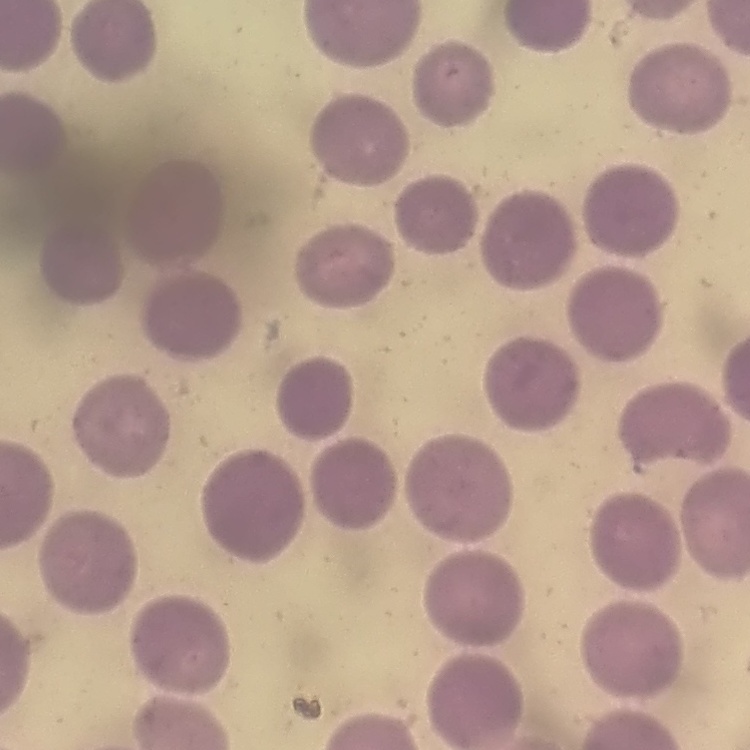
{
  "red_blood_cell_morphology": "no rouleaux formation",
  "stain": "Field's or Giemsa",
  "preparation": "thin blood smear",
  "image_type": "square crop of a larger photomicrograph"
}